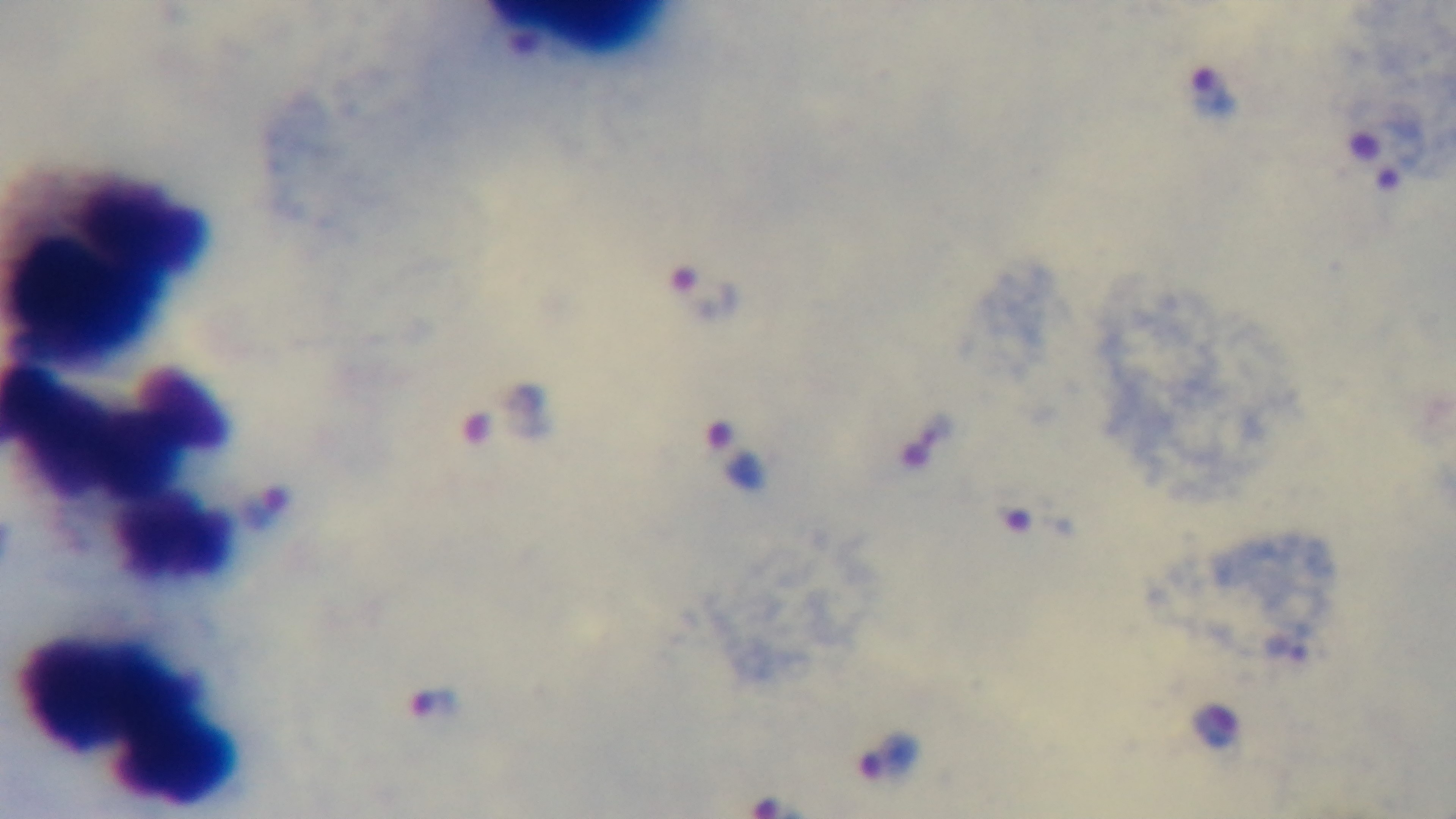

preparation = thick
objective = 100x oil immersion
malaria status = positive
stain = Giemsa
modality = light microscopy
capture = mounted 4K digital camera
field of view = one from the slide